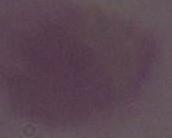

{
  "identification": "red blood cell",
  "magnification": "1000x",
  "modality": "photomicrograph"
}